Report the malaria status of this cell.
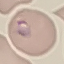

Parasitized.

Cell patch, automatically extracted from a larger field of view and resized to 64 × 64 pixels. Thin blood film. Photographed with a smartphone camera at the microscope eyepiece. Giemsa stain.